Assess this cell for malaria.
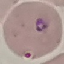
Parasitized.

Summary:
  - Capture: smartphone through the microscope eyepiece
  - Stain: Giemsa
  - Image type: automatically extracted cell patch, resized to 64 × 64 pixels
  - Preparation: thin smear